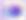

Toxoplasma gondii is seen. Captured at 400x magnification. Micrograph.